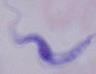

Summary:
  - Magnification: 1000x
  - Identification: trypanosome
  - Modality: micrograph